Name the parasite shown.
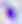
This is Toxoplasma gondii.

Micrograph. Captured at 400x magnification.